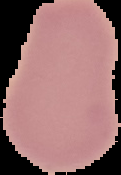

Summary:
  - Image type: segmented cell region with the area outside set to black
  - Result: negative for Plasmodium parasites
  - Preparation: thin blood smear
  - Image size: 121×175 pixels